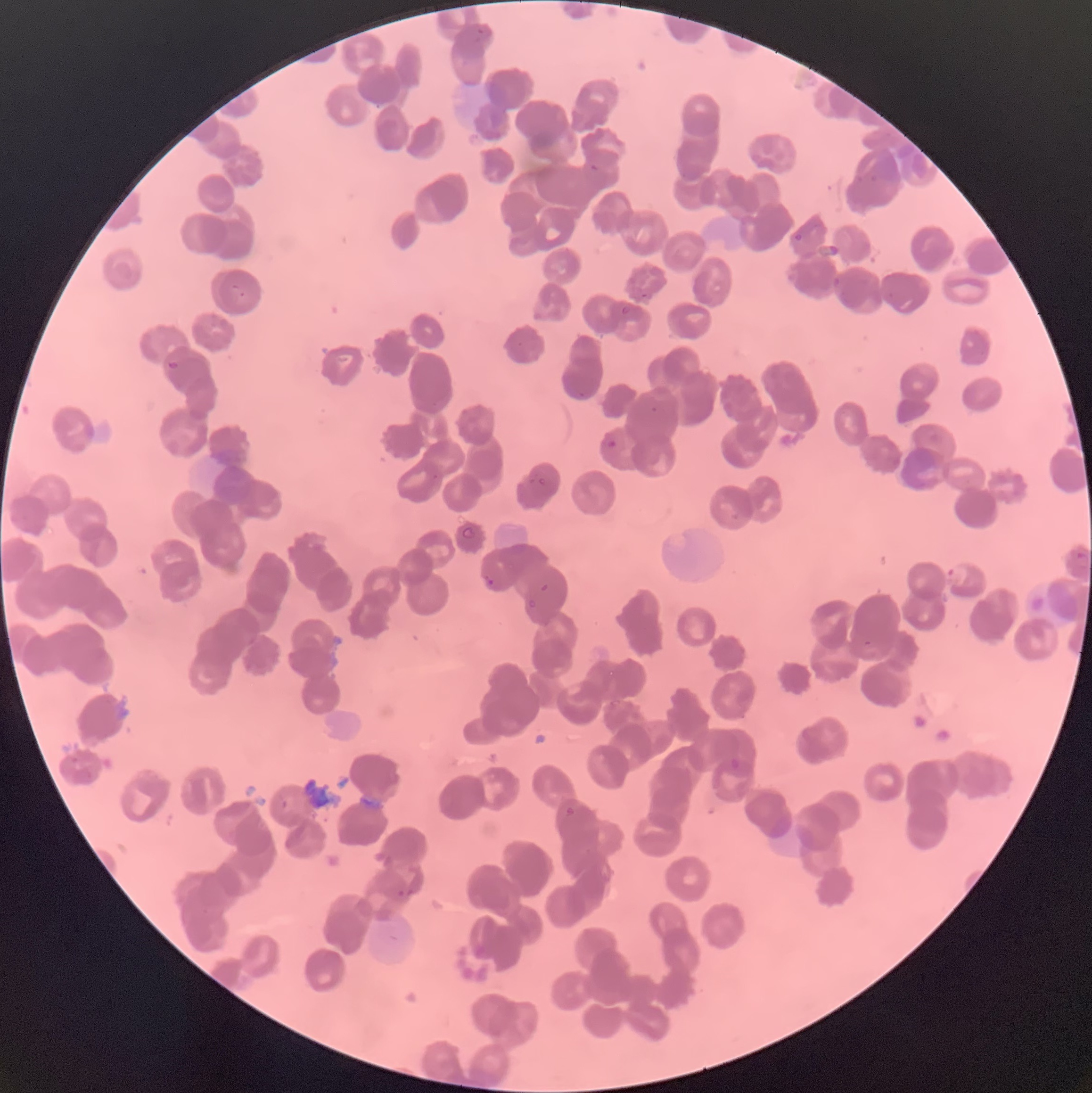
{
  "plasmodium_parasite_locations": "approximate bounding boxes as (x1, y1, x2, y2) in pixels: (474, 26, 493, 45), (589, 163, 599, 173), (869, 174, 879, 182), (793, 233, 803, 241), (830, 277, 844, 290), (232, 284, 245, 299), (640, 292, 653, 301), (619, 304, 633, 316), (166, 360, 181, 371), (572, 390, 587, 399), (650, 405, 658, 413), (601, 439, 617, 453), (537, 476, 548, 488), (460, 526, 477, 541), (1075, 549, 1089, 570), (948, 566, 969, 585), (482, 574, 494, 587), (540, 583, 549, 592), (528, 598, 538, 610), (863, 640, 875, 648), (608, 699, 622, 706), (729, 755, 748, 778), (280, 798, 288, 810), (565, 806, 574, 816), (396, 888, 415, 897)",
  "red_blood_cell_morphology": "rouleaux formation",
  "plasmodium_parasites_too_small_for_a_box": "approximate centers as (x, y) in pixels: (435, 477)",
  "preparation": "thin blood smear",
  "image_size": "1092×1093 pixels",
  "modality": "light microscopy"
}